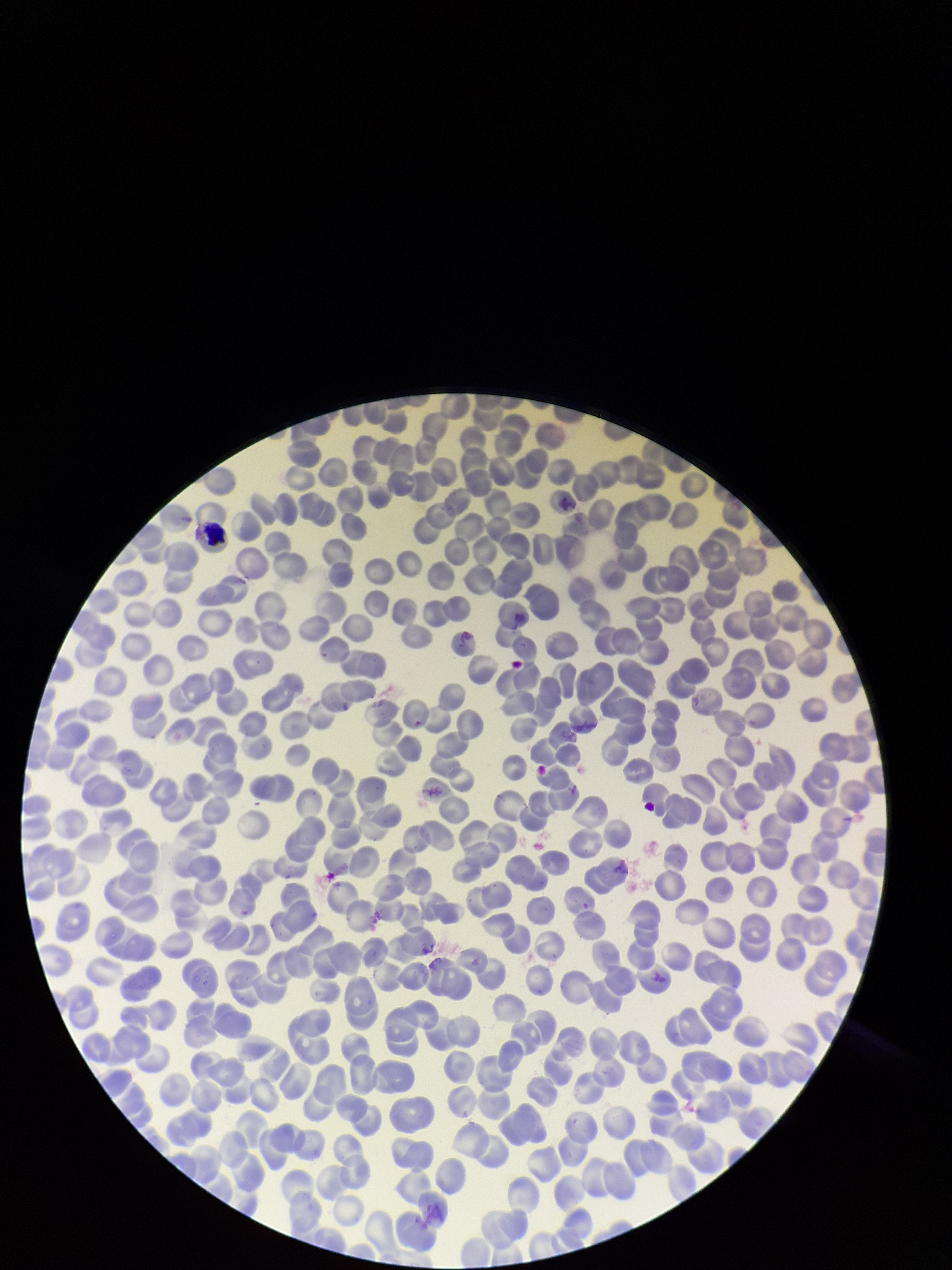 Stained with Giemsa. Image is 952×1270 pixels. Photographed through the microscope eyepiece with a smartphone camera. Parasitized red blood cells: none identified. One field from this slide. Parasitized red blood cell count: 0. Patient malaria status: negative. Preparation: thin. Red blood cell count: 328.